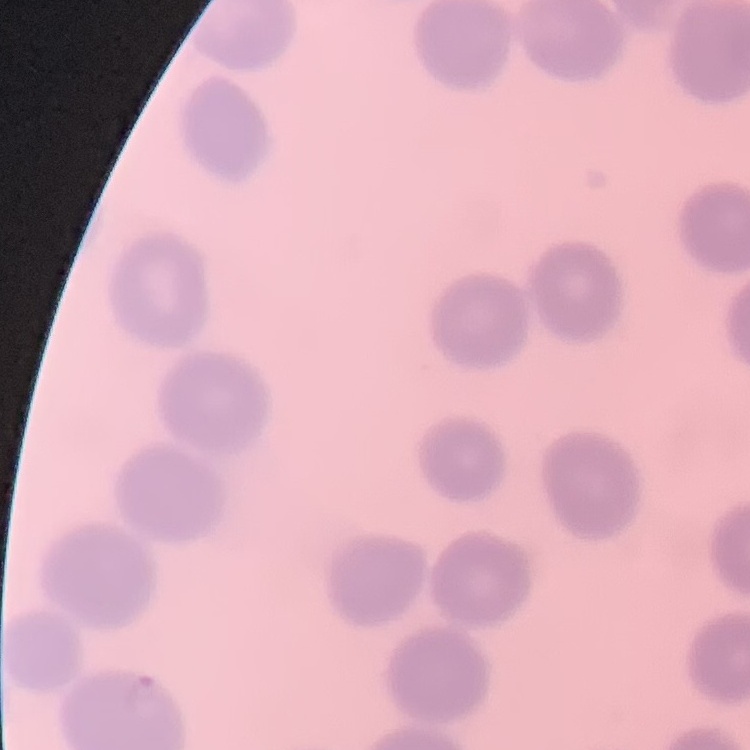

Summary:
  - Erythrocyte morphology: no rouleaux formation
  - Image type: square crop of a larger photomicrograph
  - Preparation: thin blood smear
  - Stain: Field's or Giemsa